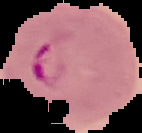

image type = cell region segmented out of the field of view; surrounding area masked to black
preparation = thin blood film
image size = 142×133 pixels
malaria status = parasitized